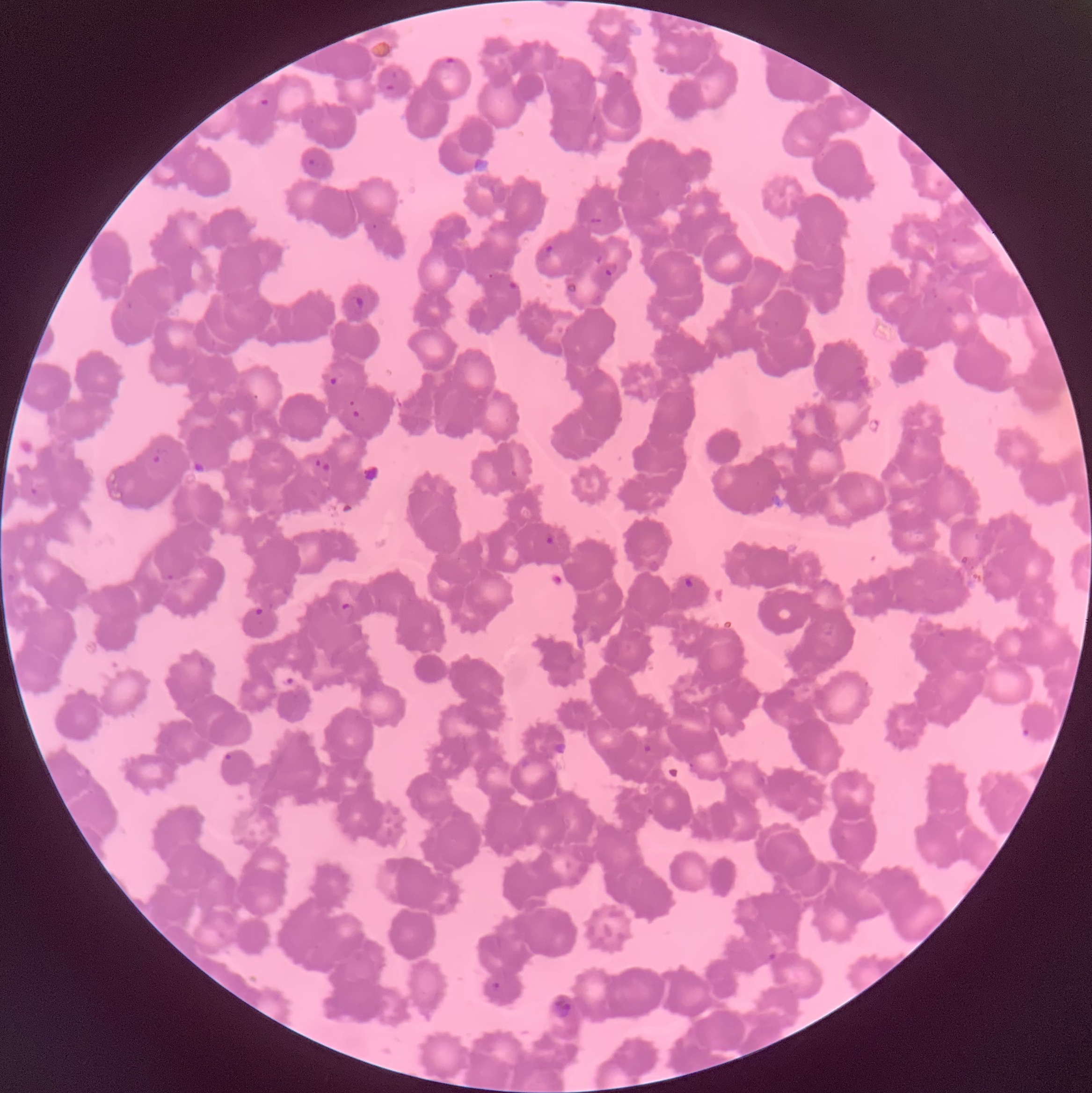 Approximate bounding boxes as (x1,y1)-(x2,y2) corner pairs in pixels. Plasmodium parasite locations: (442,57)-(459,69), (384,83)-(396,93), (258,97)-(269,107), (308,157)-(320,167), (536,245)-(554,262), (604,262)-(621,277), (508,279)-(521,294), (347,295)-(364,314), (329,376)-(338,385), (352,409)-(362,419), (152,448)-(170,464), (314,458)-(331,474), (193,459)-(208,475), (28,487)-(38,497), (544,532)-(556,545), (166,573)-(175,582), (683,576)-(695,588), (339,602)-(355,621), (253,607)-(266,617), (1020,727)-(1032,740), (641,743)-(653,755), (221,752)-(233,762), (766,952)-(777,963), (492,981)-(501,991). Thin blood film. Optical microscopy. The red blood cells show rouleaux formation. Image is 1092×1093 pixels.